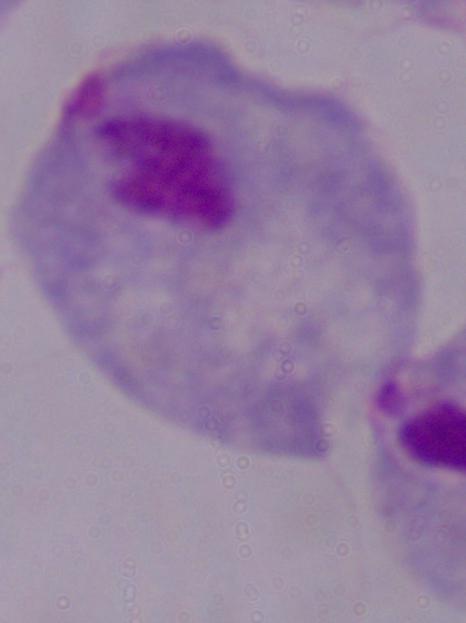
{
  "identification": "trichomonad",
  "modality": "photomicrograph",
  "magnification": "1000x"
}